Locate every blood parasite and identify its species.
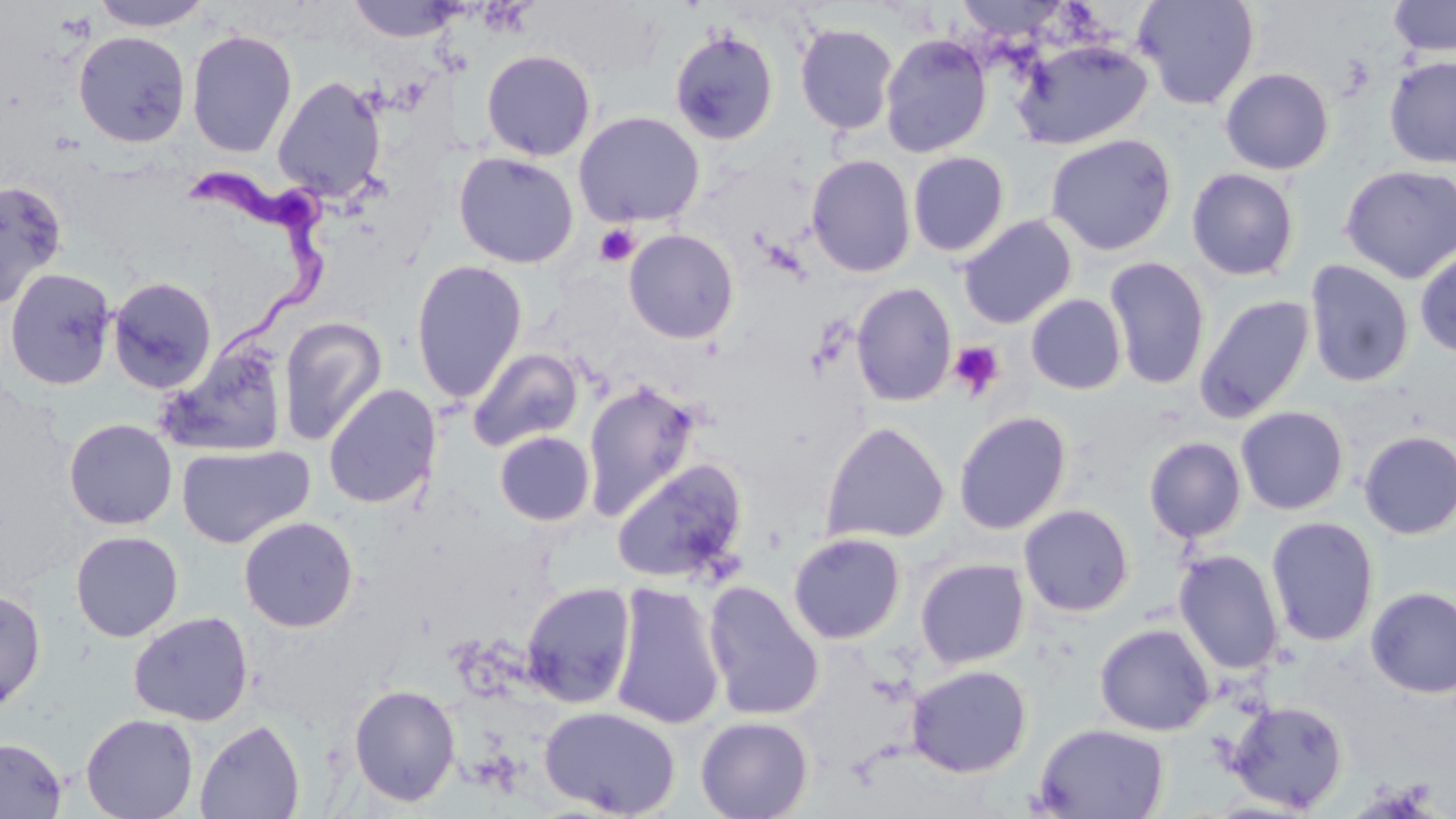

Approximate bounding boxes as (x1,y1)-(x2,y2) corner pairs in pixels.
Trypanosoma brucei: (186,161)-(332,379).
No Plasmodium falciparum, Plasmodium ovale, Plasmodium malariae, Plasmodium vivax, or Babesia divergens observed.

slide-level diagnosis = Trypanosoma brucei
uninfected red blood cell locations = approximate bounding boxes as (x1,y1)-(x2,y2) corner pairs in pixels: (88,0)-(213,31), (346,0)-(460,43), (1132,0)-(1260,111), (1387,0)-(1455,57), (795,23)-(898,135), (668,28)-(780,145), (186,29)-(298,159), (73,30)-(191,147), (879,33)-(993,158), (1012,38)-(1154,149), (480,49)-(596,161), (1384,55)-(1456,169), (1219,67)-(1335,176), (272,76)-(387,204), (573,111)-(705,228), (1045,134)-(1177,256), (453,152)-(579,268), (907,152)-(1010,257), (806,153)-(916,277), (1339,164)-(1456,284), (1186,167)-(1300,281), (0,179)-(67,309), (958,215)-(1077,329), (623,228)-(740,344), (1414,243)-(1456,359), (1104,256)-(1211,390), (1304,259)-(1415,388), (410,260)-(528,404), (3,267)-(117,391), (107,276)-(217,394), (851,282)-(957,407), (1025,293)-(1127,395), (1195,294)-(1316,422), (278,316)-(388,446), (156,342)-(291,457), (467,347)-(585,453), (582,381)-(702,521), (323,383)-(442,510), (1235,406)-(1349,515), (953,410)-(1072,535), (64,418)-(177,529), (820,421)-(949,545), (1357,430)-(1456,540), (494,431)-(595,526), (1144,437)-(1247,543), (176,444)-(313,549), (611,458)-(749,586), (1018,503)-(1135,617), (238,516)-(359,632), (1265,516)-(1380,647), (69,530)-(184,642), (788,532)-(906,644), (1172,549)-(1285,675), (915,558)-(1030,669), (609,581)-(726,731), (703,581)-(825,721), (520,582)-(637,708), (0,587)-(47,712), (1365,587)-(1456,698), (128,611)-(254,726), (1094,622)-(1215,736), (905,664)-(1032,778), (349,684)-(461,807), (1225,699)-(1348,813), (539,706)-(681,817), (81,713)-(198,819), (695,715)-(814,819), (194,719)-(305,818), (1033,722)-(1170,818), (0,736)-(67,819)
platelet locations = approximate bounding boxes as (x1,y1)-(x2,y2) corner pairs in pixels: (594,224)-(640,268), (948,341)-(1005,400)
magnification = 1000x
modality = light microscopy
stain = May-Grünwald-Giemsa
image size = 1456×819 pixels
preparation = thin blood smear
field of view = single